Classify this cell by malaria status.
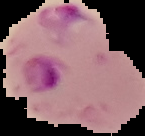
Parasitized.

From a thin blood smear. Image is 145×136 pixels. The area outside the segmented cell region is set to black.